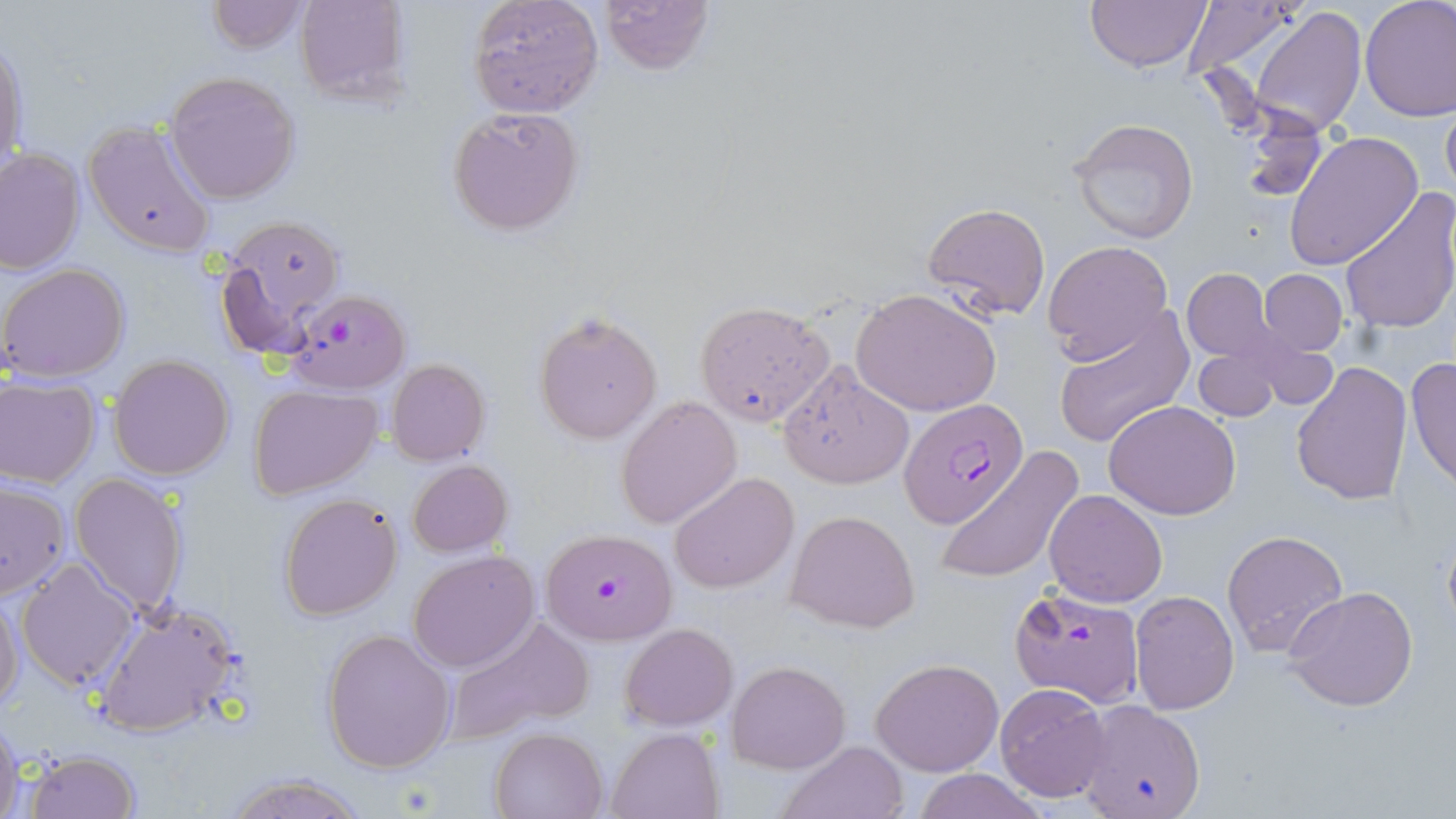
Summary:
  - Coordinate format: approximate bounding boxes as [x1, y1, x2, y2] in pixels
  - Plasmodium falciparum-infected red blood cell locations: [284, 289, 410, 396], [899, 400, 1028, 528], [539, 528, 678, 646], [1010, 587, 1147, 706]
  - Uninfected red blood cell locations: [293, 0, 410, 106], [467, 0, 603, 117], [600, 0, 715, 75], [1085, 0, 1211, 71], [1360, 0, 1456, 121], [205, 1, 308, 54], [1178, 1, 1305, 87], [1250, 6, 1366, 136], [1, 35, 26, 177], [164, 71, 302, 204], [1439, 96, 1456, 204], [447, 107, 586, 235], [1068, 117, 1200, 245], [82, 118, 219, 259], [1284, 130, 1425, 269], [0, 148, 85, 276], [1339, 188, 1456, 336], [922, 202, 1050, 321], [214, 212, 346, 352], [1043, 240, 1174, 362], [1, 262, 130, 383], [1182, 269, 1279, 363], [1259, 269, 1348, 356], [852, 288, 1002, 417], [695, 300, 834, 427], [534, 309, 662, 443], [1052, 312, 1194, 450], [1192, 346, 1281, 421], [107, 355, 234, 480], [1406, 356, 1456, 489], [387, 359, 489, 466], [1291, 361, 1414, 507], [778, 364, 913, 490], [1, 376, 101, 487], [249, 385, 383, 498], [616, 397, 743, 529], [1104, 401, 1242, 519], [935, 449, 1083, 585], [407, 459, 513, 558], [669, 472, 799, 595], [70, 473, 192, 618], [0, 480, 70, 600], [1045, 489, 1166, 607], [277, 492, 403, 621], [786, 509, 920, 633], [1221, 530, 1349, 659], [408, 551, 538, 671], [16, 557, 140, 693], [1283, 585, 1419, 713], [1129, 591, 1241, 714], [0, 592, 23, 714], [92, 599, 244, 738], [443, 615, 594, 745], [620, 623, 737, 730], [321, 628, 457, 773], [871, 657, 1004, 776], [727, 660, 851, 773], [994, 683, 1113, 802], [1075, 700, 1208, 819], [0, 710, 23, 819], [490, 727, 607, 818], [607, 727, 725, 819], [776, 739, 910, 819], [23, 748, 141, 818], [910, 769, 1048, 819], [220, 772, 369, 818]
  - Slide-level diagnosis: Plasmodium falciparum
  - Modality: light microscopy
  - Field of view: one of a larger specimen
  - Magnification: 1000x
  - Preparation: thin blood film
  - Stain: May-Grünwald-Giemsa
  - Image size: 1456×819 pixels